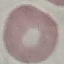

Summary:
  - Result: negative for malaria parasites
  - Preparation: thin blood film
  - Image type: cell patch, automatically extracted from a larger field of view and resized to 64 × 64 pixels
  - Capture: smartphone through the microscope eyepiece
  - Stain: Giemsa